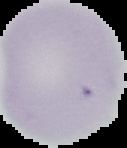

preparation = thin blood smear
image size = 127×148 pixels
malaria status = uninfected
image type = segmented cell region with the area outside set to black